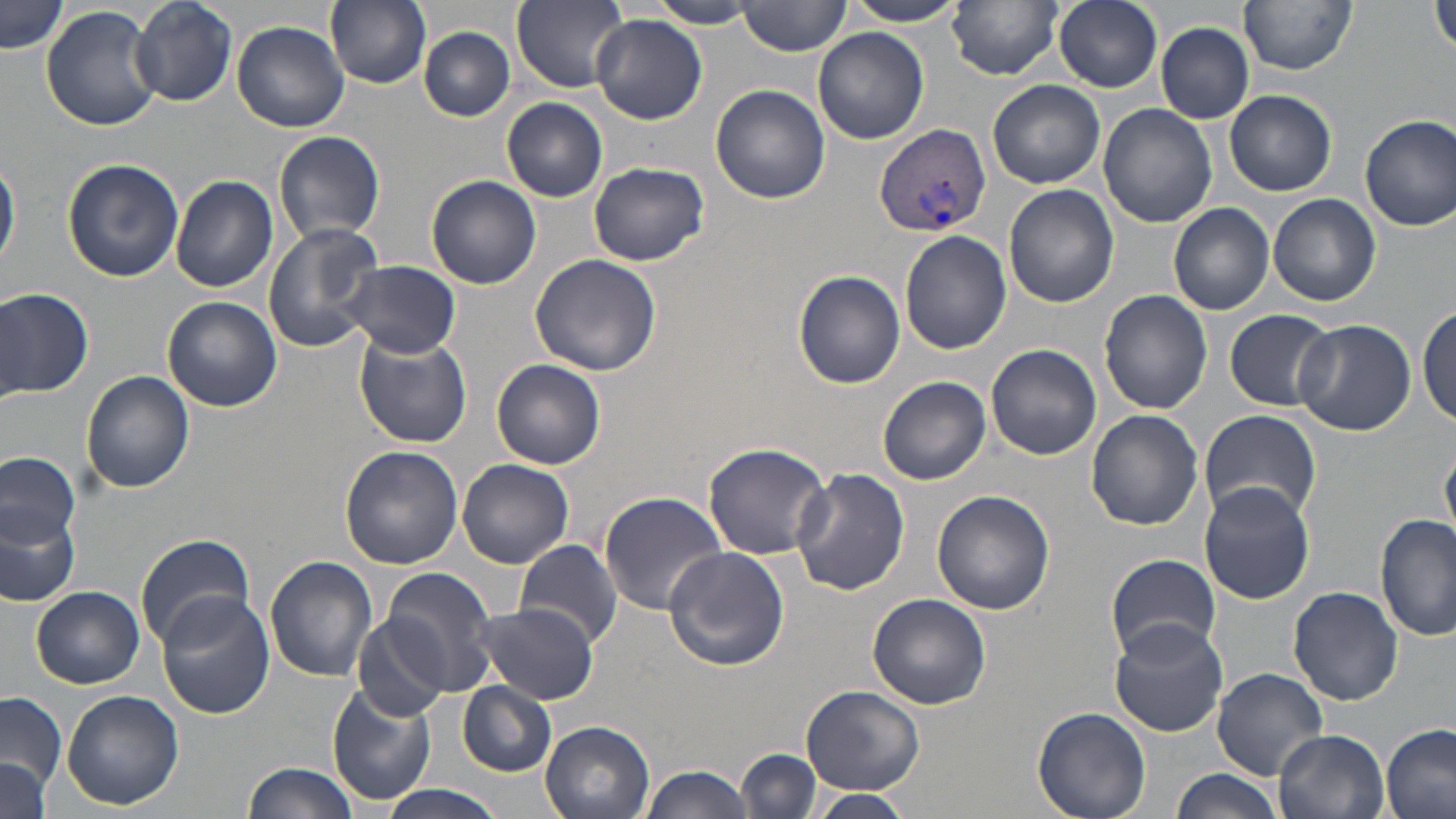

Summary:
  - Coordinate format: approximate bounding boxes as [x1, y1, x2, y2] in pixels
  - Uninfected red blood cell locations: [127, 0, 237, 108], [325, 0, 431, 89], [512, 0, 628, 91], [841, 0, 971, 25], [948, 0, 1064, 78], [1053, 0, 1163, 91], [1239, 0, 1357, 74], [1432, 0, 1456, 60], [1, 1, 68, 56], [647, 1, 759, 28], [738, 1, 850, 56], [43, 6, 160, 130], [592, 15, 706, 124], [231, 20, 349, 130], [1156, 21, 1255, 123], [419, 27, 515, 120], [813, 28, 928, 145], [770, 40, 898, 162], [988, 79, 1105, 188], [710, 84, 830, 204], [1225, 90, 1336, 196], [502, 98, 608, 202], [1098, 103, 1216, 228], [1360, 114, 1456, 229], [274, 131, 385, 243], [0, 150, 20, 275], [61, 157, 184, 283], [588, 161, 709, 267], [170, 175, 279, 292], [427, 176, 541, 289], [1004, 185, 1119, 309], [1267, 193, 1381, 308], [1168, 202, 1275, 316], [262, 222, 387, 351], [899, 230, 1010, 353], [528, 252, 661, 375], [338, 259, 459, 360], [793, 270, 906, 389], [0, 286, 94, 400], [1100, 289, 1212, 414], [162, 296, 282, 411], [1417, 303, 1456, 429], [1225, 309, 1336, 412], [1293, 319, 1416, 436], [352, 327, 472, 448], [986, 343, 1100, 460], [491, 359, 607, 471], [81, 370, 194, 493], [878, 376, 991, 485], [1200, 407, 1321, 524], [1086, 410, 1203, 531], [703, 442, 831, 559], [339, 446, 464, 570], [1441, 449, 1456, 538], [0, 453, 81, 548], [457, 458, 574, 568], [792, 467, 910, 596], [1198, 481, 1316, 605], [930, 490, 1055, 615], [598, 491, 728, 614], [0, 507, 76, 608], [1376, 514, 1456, 643], [134, 533, 254, 649], [516, 540, 624, 647], [663, 546, 790, 671], [1106, 552, 1222, 660], [265, 554, 377, 682], [373, 567, 501, 699], [30, 584, 144, 688], [1288, 586, 1404, 704], [154, 592, 275, 719], [868, 593, 992, 710], [474, 604, 597, 703], [349, 615, 452, 722], [1109, 620, 1229, 736], [1212, 668, 1328, 780], [327, 684, 438, 805], [457, 684, 555, 775], [800, 685, 924, 795], [61, 688, 184, 810], [0, 692, 67, 800], [1032, 707, 1152, 819], [540, 720, 655, 819], [1383, 725, 1455, 819], [1275, 728, 1391, 818], [738, 748, 822, 818], [0, 757, 49, 818], [243, 760, 362, 819], [642, 764, 756, 819], [1168, 769, 1283, 819], [377, 786, 510, 819], [806, 790, 917, 817]
  - Plasmodium vivax-infected red blood cell locations: [873, 122, 991, 237]
  - Slide-level diagnosis: Plasmodium vivax
  - Modality: optical microscopy
  - Preparation: thin blood film
  - Stain: May-Grünwald-Giemsa
  - Magnification: 1000x
  - Image size: 1456×819 pixels
  - Field of view: one of a larger specimen